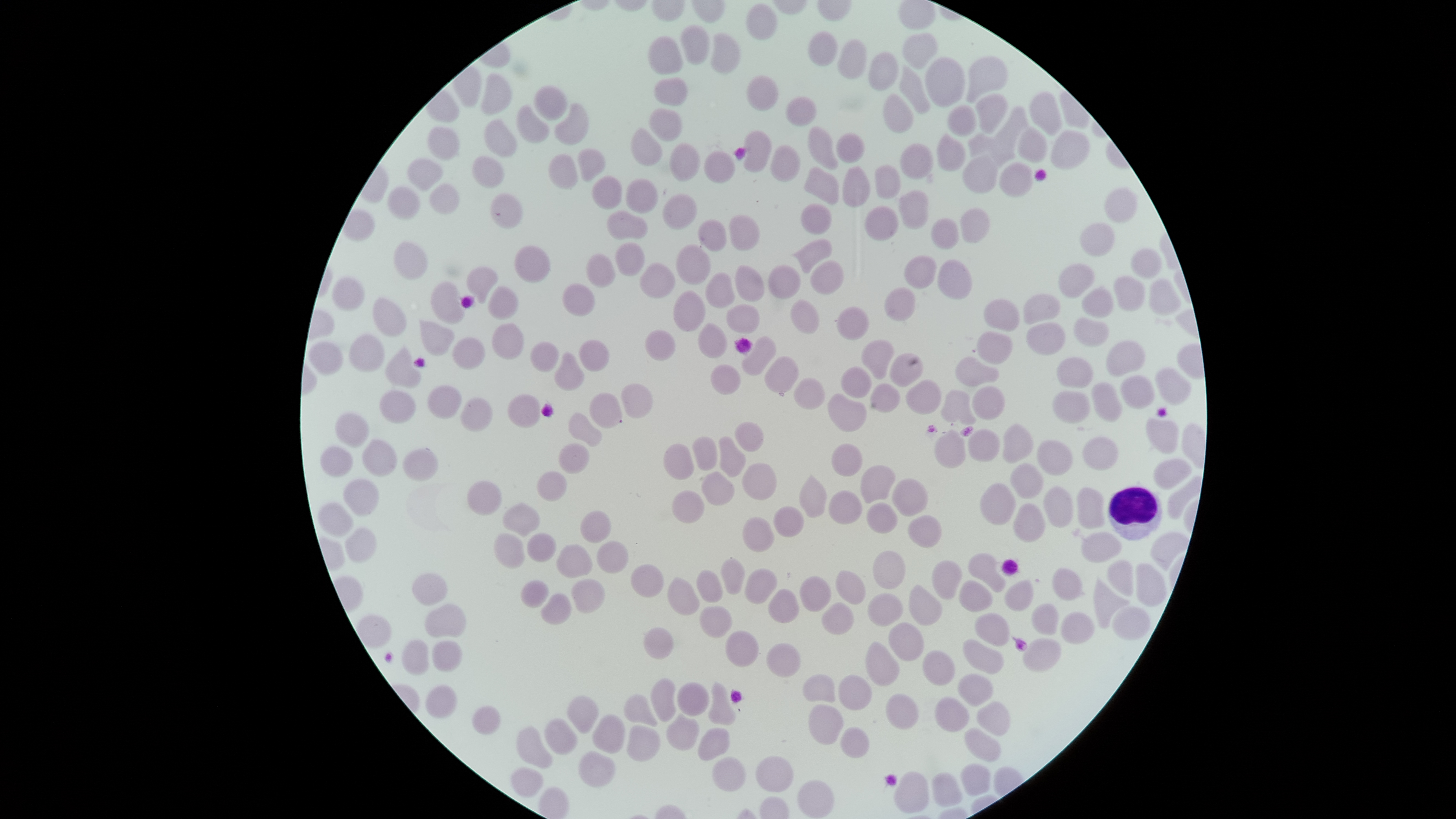 Approximate bounding boxes as [left, top, right, bottom] in pixels. WBCs: [1107, 486, 1163, 540]. Uninfected RBCs: [746, 4, 778, 39], [679, 25, 709, 65], [808, 30, 838, 66], [710, 33, 740, 74], [903, 33, 938, 69], [648, 36, 683, 75], [837, 39, 866, 79], [867, 52, 899, 91], [925, 56, 965, 107], [966, 56, 1008, 104], [900, 66, 930, 114], [481, 73, 512, 115], [746, 75, 779, 112], [654, 77, 688, 106], [533, 84, 567, 120], [1029, 91, 1063, 136], [883, 93, 914, 133], [975, 93, 1008, 134], [785, 96, 817, 127], [554, 103, 589, 146], [516, 105, 549, 143], [946, 105, 977, 137], [995, 106, 1028, 147], [648, 108, 682, 142], [484, 119, 517, 158], [427, 126, 460, 160], [808, 126, 839, 170], [630, 127, 662, 166], [1017, 127, 1047, 163], [743, 129, 772, 173], [1050, 129, 1090, 169], [836, 132, 866, 163], [967, 133, 1015, 168], [937, 134, 967, 172], [669, 142, 701, 182], [899, 143, 933, 180], [770, 144, 801, 182], [577, 147, 606, 182], [703, 150, 736, 183], [548, 154, 578, 190], [962, 154, 999, 194], [472, 155, 504, 188], [407, 158, 443, 192], [999, 162, 1033, 197], [874, 164, 901, 199], [843, 165, 871, 207], [804, 167, 839, 205], [591, 175, 622, 209], [625, 177, 658, 213], [429, 183, 459, 214], [387, 187, 420, 220], [1104, 187, 1138, 224], [898, 189, 929, 229], [490, 192, 523, 229], [662, 193, 697, 230], [799, 203, 833, 234], [864, 206, 899, 240], [960, 208, 990, 243], [606, 210, 648, 240], [729, 214, 760, 251], [930, 218, 959, 250], [698, 219, 727, 252], [1080, 222, 1115, 256], [791, 238, 832, 273], [394, 241, 428, 280], [615, 242, 645, 276], [514, 244, 551, 283], [676, 244, 711, 285], [1130, 248, 1162, 278], [585, 253, 616, 288], [904, 255, 937, 289], [937, 259, 972, 299], [810, 260, 844, 295], [639, 263, 676, 299], [1058, 263, 1095, 298], [767, 264, 801, 298], [735, 265, 765, 302], [465, 267, 497, 304], [705, 272, 735, 308], [1112, 275, 1145, 311], [331, 277, 365, 310], [1149, 278, 1181, 316], [430, 281, 465, 325], [562, 283, 595, 317], [488, 285, 519, 320], [1081, 286, 1114, 318], [884, 287, 916, 322], [673, 290, 706, 332], [1022, 294, 1060, 325], [372, 297, 406, 336], [790, 299, 820, 333], [983, 299, 1020, 332], [727, 304, 760, 334], [836, 306, 870, 341], [1073, 317, 1109, 347], [419, 319, 455, 356], [1026, 322, 1066, 356], [491, 323, 525, 360], [698, 323, 728, 358], [645, 329, 676, 361], [976, 330, 1013, 364], [347, 333, 385, 372], [452, 336, 485, 370], [741, 336, 777, 375], [578, 339, 610, 372], [862, 339, 895, 380], [1105, 340, 1146, 377], [308, 341, 343, 376], [530, 341, 559, 372], [385, 345, 421, 388], [554, 351, 584, 391], [889, 353, 923, 387], [764, 355, 800, 396], [955, 356, 1000, 387], [1056, 357, 1094, 388], [710, 364, 741, 395], [841, 365, 872, 399], [1155, 367, 1192, 405], [1120, 375, 1155, 409], [794, 377, 826, 410], [905, 379, 942, 414], [1091, 382, 1123, 423], [621, 383, 653, 418], [869, 383, 901, 413], [426, 385, 462, 419], [972, 386, 1005, 421], [378, 390, 416, 423], [941, 390, 976, 426], [1051, 391, 1090, 424], [590, 392, 622, 429], [827, 393, 866, 432], [507, 394, 541, 429], [460, 397, 492, 432], [568, 412, 602, 448], [334, 413, 369, 448], [1145, 417, 1179, 454], [735, 421, 764, 452], [1002, 423, 1034, 463], [967, 428, 1000, 463], [934, 429, 966, 469], [691, 436, 718, 470], [718, 436, 746, 477], [1082, 436, 1118, 470], [362, 439, 397, 477], [1036, 439, 1073, 476], [558, 443, 590, 475], [663, 443, 694, 480], [831, 443, 863, 477], [319, 445, 354, 477], [403, 448, 439, 482], [1152, 457, 1192, 490], [742, 462, 777, 501], [1009, 462, 1044, 499], [861, 465, 896, 504], [537, 470, 567, 501], [701, 471, 735, 506], [799, 473, 827, 519], [342, 478, 379, 517], [891, 478, 928, 518], [466, 480, 502, 516], [979, 482, 1016, 526], [1043, 485, 1074, 528], [1076, 486, 1106, 529], [671, 490, 705, 524], [829, 490, 863, 524], [502, 502, 540, 537], [866, 502, 898, 534], [317, 503, 354, 537], [1013, 503, 1046, 542], [773, 505, 804, 537], [581, 510, 611, 543], [908, 515, 942, 548], [742, 517, 775, 553], [346, 527, 377, 563], [527, 532, 556, 562], [1081, 532, 1122, 563], [1150, 532, 1188, 571], [493, 533, 525, 569], [596, 541, 629, 574], [556, 543, 593, 578], [872, 550, 906, 589], [967, 553, 1006, 593], [720, 558, 745, 595], [1106, 559, 1134, 596], [931, 560, 963, 599], [1135, 562, 1167, 607], [630, 564, 664, 597], [1051, 567, 1085, 601], [744, 568, 777, 604], [696, 569, 723, 602], [836, 570, 866, 605], [411, 572, 448, 605], [799, 575, 831, 612], [667, 577, 699, 616], [1093, 577, 1131, 629], [570, 578, 605, 614], [1004, 579, 1034, 611], [520, 580, 549, 609], [959, 580, 993, 612], [908, 584, 943, 626], [768, 589, 800, 623], [541, 593, 572, 625], [867, 593, 903, 627], [821, 602, 854, 635], [425, 603, 466, 638], [1031, 603, 1059, 635], [699, 605, 733, 639], [1111, 606, 1150, 640], [974, 612, 1010, 646], [1060, 612, 1095, 644], [356, 615, 391, 649], [888, 622, 924, 662], [643, 627, 674, 660], [725, 630, 759, 668], [1022, 638, 1062, 673], [962, 639, 1005, 674], [401, 640, 429, 676], [432, 641, 461, 672], [864, 641, 900, 686], [766, 643, 801, 677], [922, 650, 956, 686], [802, 673, 836, 703], [957, 673, 994, 706], [838, 674, 873, 710], [650, 678, 677, 722], [708, 680, 736, 726], [676, 682, 709, 717], [425, 685, 457, 719], [885, 693, 919, 729], [623, 694, 657, 727], [566, 696, 599, 734], [934, 696, 970, 732], [977, 701, 1011, 736], [808, 704, 844, 745], [472, 706, 501, 735], [592, 714, 625, 754], [666, 714, 700, 751], [544, 718, 579, 755], [516, 726, 553, 768], [627, 726, 661, 762], [840, 726, 870, 758], [698, 727, 730, 761], [964, 727, 1001, 761], [578, 750, 616, 787], [755, 755, 794, 793], [711, 756, 746, 792], [960, 763, 990, 795], [511, 767, 544, 796], [893, 771, 930, 813], [931, 772, 963, 807], [797, 779, 835, 818]. One field of view of the specimen. Image is 1456×819 pixels. Thin blood film. Smartphone photograph through the microscope eyepiece. Presence: no malaria parasites detected. The visible region is circular. Giemsa stain.